Outline each blood parasite and name the species.
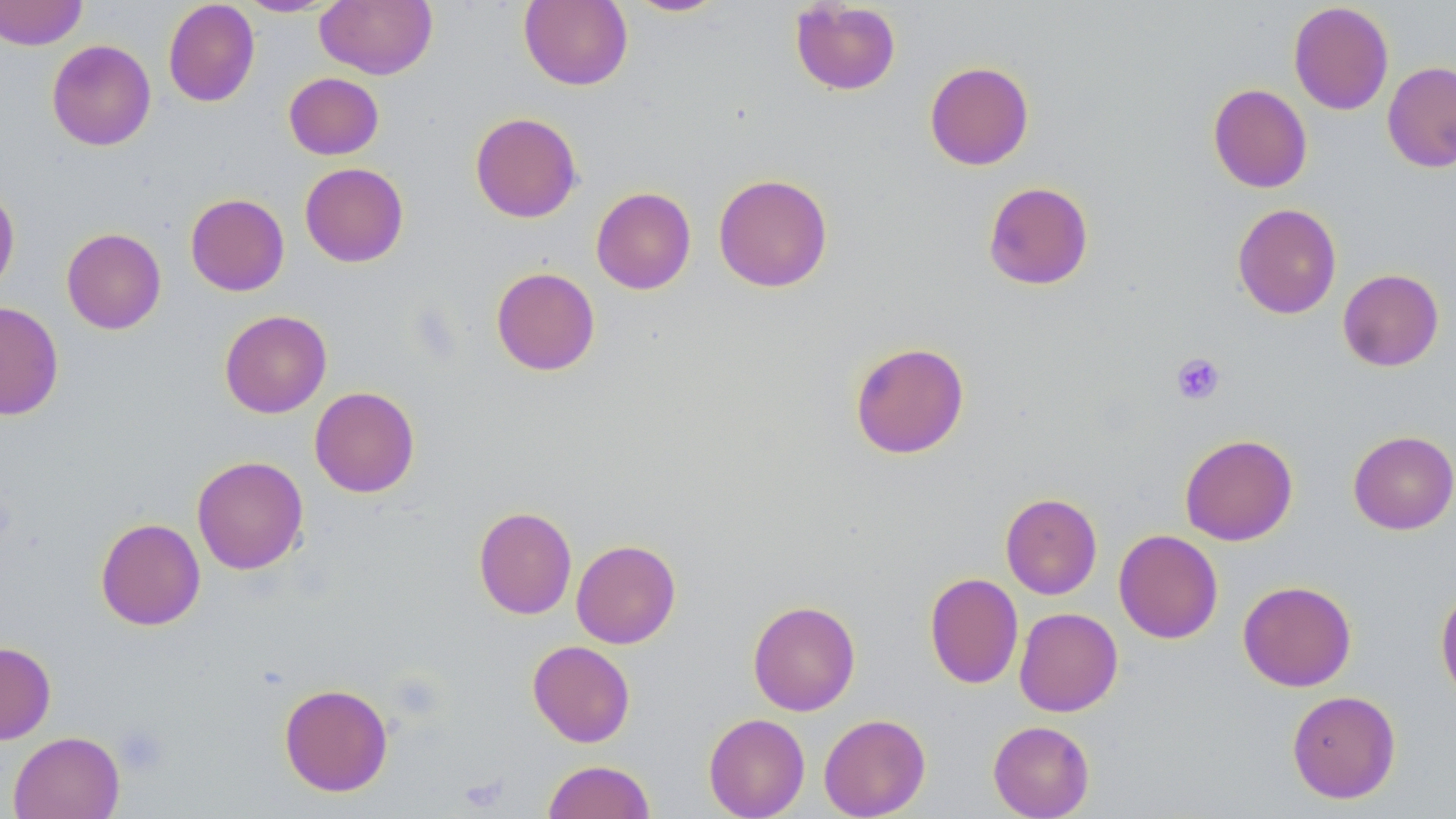

No blood parasites seen.

Summary:
  - Coordinate format: approximate bounding boxes as [x1, y1, x2, y2] in pixels
  - Platelet locations: [1171, 352, 1226, 405], [115, 725, 170, 777]
  - Uninfected red blood cell locations: [0, 0, 88, 50], [236, 0, 339, 16], [315, 0, 437, 79], [518, 0, 633, 91], [624, 0, 728, 17], [162, 1, 260, 107], [789, 1, 902, 96], [1288, 2, 1394, 115], [46, 39, 156, 151], [924, 61, 1034, 170], [1382, 61, 1456, 172], [283, 72, 384, 160], [1207, 84, 1312, 193], [470, 112, 582, 223], [299, 162, 409, 267], [713, 173, 833, 293], [982, 181, 1093, 290], [0, 182, 20, 293], [591, 187, 696, 294], [185, 193, 289, 296], [1232, 203, 1342, 319], [61, 227, 166, 334], [491, 267, 601, 376], [1337, 268, 1444, 372], [0, 301, 64, 420], [219, 310, 332, 418], [849, 341, 969, 459], [309, 386, 420, 497], [1348, 430, 1456, 534], [1180, 433, 1298, 546], [192, 455, 309, 575], [1000, 493, 1102, 600], [474, 505, 577, 619], [95, 518, 205, 630], [1113, 529, 1223, 644], [571, 539, 681, 649], [924, 572, 1023, 689], [1237, 580, 1357, 691], [1435, 587, 1456, 707], [748, 600, 860, 715], [1014, 607, 1123, 716], [527, 640, 635, 747], [0, 641, 56, 744], [279, 683, 393, 796], [1287, 690, 1401, 803], [703, 713, 810, 819], [819, 713, 931, 818], [988, 720, 1095, 819], [8, 731, 125, 819], [542, 760, 655, 819]
  - Slide-level diagnosis: no evidence of blood parasites
  - Preparation: thin blood film
  - Modality: optical microscopy
  - Magnification: 1000x
  - Image size: 1456×819 pixels
  - Field of view: one of a larger specimen
  - Stain: May-Grünwald-Giemsa